Classify this cell by malaria status.
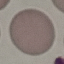

It is uninfected.

Thin smear of blood. Photographed with a smartphone camera at the microscope eyepiece. Cell patch, automatically extracted from a larger field of view and resized to 64 × 64 pixels. Giemsa stain.